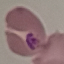

malaria status = parasitized
preparation = thin smear
stain = Giemsa
capture = smartphone through the microscope eyepiece
image type = cell patch, automatically extracted from a larger field of view and resized to 64 × 64 pixels